Locate and identify every blood parasite.
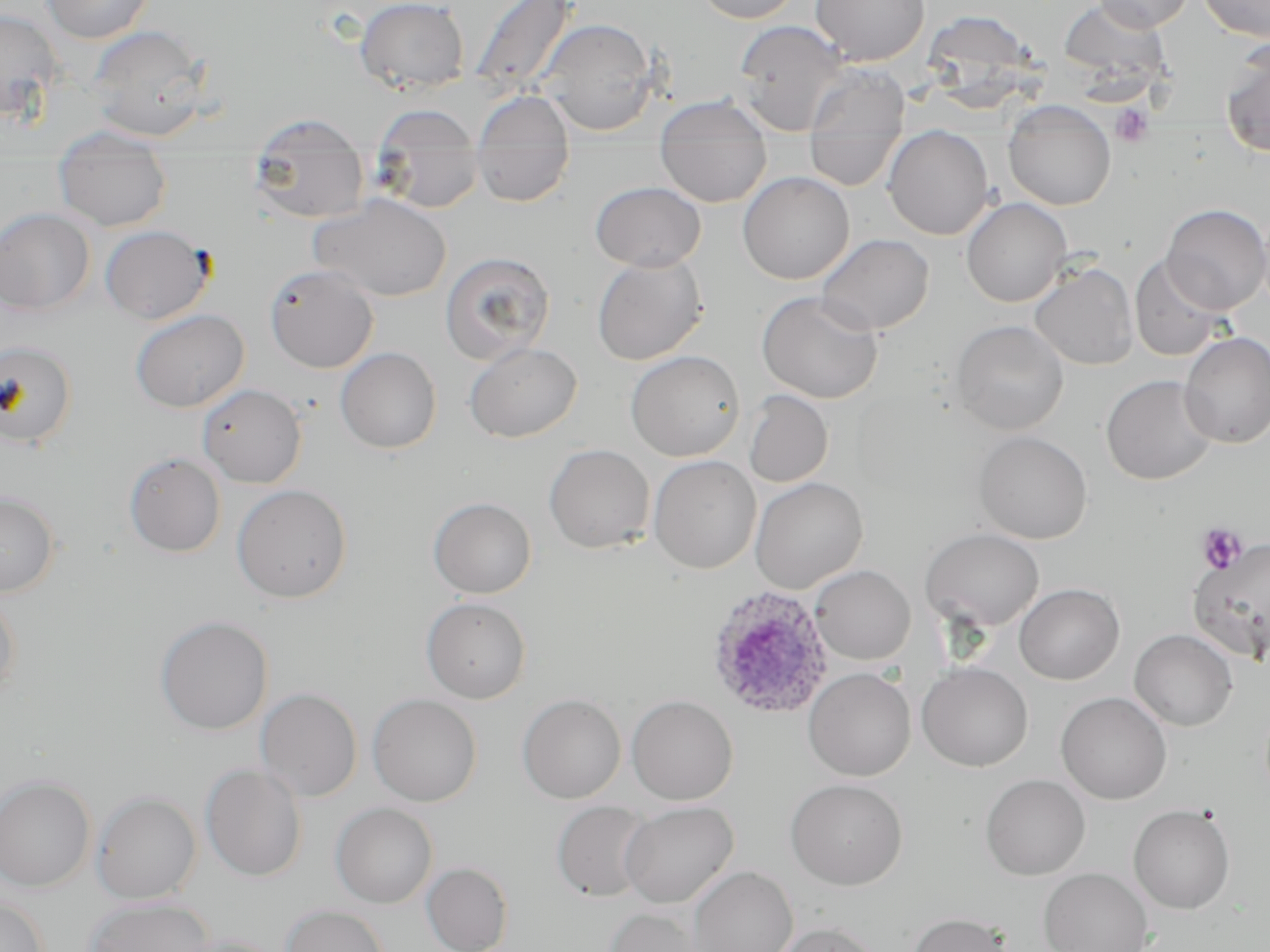

Approximate bounding boxes as (x1, y1, x2, y2) in pixels.
Plasmodium ovale-infected red blood cells: (707, 585, 833, 719).
No Plasmodium falciparum, Plasmodium malariae, Plasmodium vivax, Babesia divergens, or Trypanosoma brucei observed.

Platelet locations: (1110, 103, 1155, 147), (1196, 523, 1248, 574). Uninfected red blood cell locations: (40, 0, 154, 44), (355, 0, 469, 94), (467, 0, 578, 97), (693, 0, 802, 24), (810, 0, 929, 65), (1093, 0, 1193, 32), (1198, 0, 1270, 41), (1061, 3, 1171, 98), (0, 9, 66, 123), (931, 12, 1053, 111), (537, 18, 658, 135), (733, 20, 852, 136), (86, 24, 213, 142), (1220, 43, 1270, 158), (803, 62, 910, 172), (475, 90, 574, 147), (653, 95, 771, 142), (1003, 99, 1116, 210), (372, 104, 480, 149), (247, 112, 365, 151), (804, 124, 905, 192), (49, 125, 173, 156), (883, 125, 994, 240), (656, 140, 771, 206), (470, 147, 575, 207), (377, 151, 486, 213), (249, 152, 371, 224), (54, 157, 172, 231), (737, 171, 855, 284), (590, 181, 706, 272), (309, 194, 452, 302), (961, 198, 1071, 307), (1162, 204, 1270, 314), (0, 208, 96, 315), (0, 215, 203, 317), (100, 225, 213, 324), (817, 234, 934, 335), (440, 251, 556, 365), (591, 254, 708, 365), (1129, 254, 1230, 362), (1030, 262, 1138, 370), (264, 264, 379, 373), (757, 290, 884, 403), (130, 309, 249, 413), (951, 319, 1069, 435), (1179, 332, 1270, 448), (0, 341, 78, 449), (464, 342, 582, 442), (335, 347, 442, 454), (625, 350, 745, 461), (1100, 375, 1216, 485), (197, 383, 307, 488), (743, 391, 833, 488), (974, 431, 1092, 544), (544, 443, 655, 554), (124, 452, 226, 557), (648, 455, 761, 574), (750, 477, 868, 593), (231, 484, 352, 603), (0, 491, 60, 597), (428, 497, 537, 599), (921, 528, 1044, 632), (1188, 538, 1270, 665), (810, 565, 915, 665), (1014, 583, 1124, 684), (0, 591, 21, 701), (421, 598, 532, 704), (155, 616, 273, 735), (1129, 629, 1238, 731), (916, 662, 1033, 771), (804, 668, 916, 781), (255, 688, 362, 802), (1055, 691, 1172, 804), (367, 694, 482, 806), (517, 694, 626, 803), (626, 695, 738, 805), (200, 763, 307, 882), (980, 774, 1090, 880), (0, 775, 95, 891), (786, 778, 908, 890), (91, 791, 202, 904), (551, 800, 655, 903), (330, 802, 438, 908), (619, 802, 738, 908), (1128, 804, 1236, 914), (421, 862, 512, 952), (687, 866, 797, 952), (1038, 867, 1152, 952), (0, 896, 49, 952), (84, 897, 217, 952), (280, 904, 391, 952), (604, 906, 707, 952), (906, 912, 1015, 952), (772, 922, 881, 952), (172, 935, 286, 952). Slide-level diagnosis: Plasmodium ovale. Thin blood film. May-Grünwald-Giemsa-stained preparation. Image is 1270×952 pixels. Single field of view. Captured at 1000x magnification. Light microscopy.